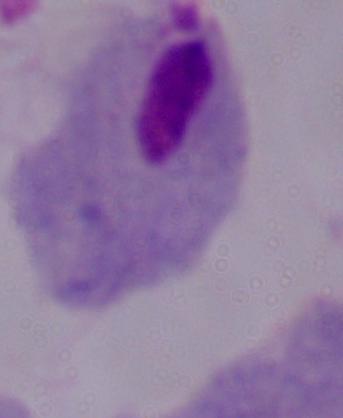
modality = micrograph
identification = trichomonad
magnification = 1000x